Assess this cell for malaria.
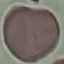

It is uninfected.

Giemsa stain. Automatically extracted cell patch, resized to 64 × 64 pixels. Thin blood film. Acquired by smartphone through the microscope eyepiece.